Assess this cell for malaria.
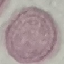
It is uninfected.

preparation = thin blood smear
stain = Giemsa
image type = cell patch, automatically extracted from a larger field of view and resized to 64 × 64 pixels
capture = smartphone through the microscope eyepiece